Classify this cell by malaria status.
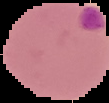
It is parasitized.

Image is 109×103 pixels. Segmented cell region on a black background. From a thin blood smear.